Locate every malaria parasite.
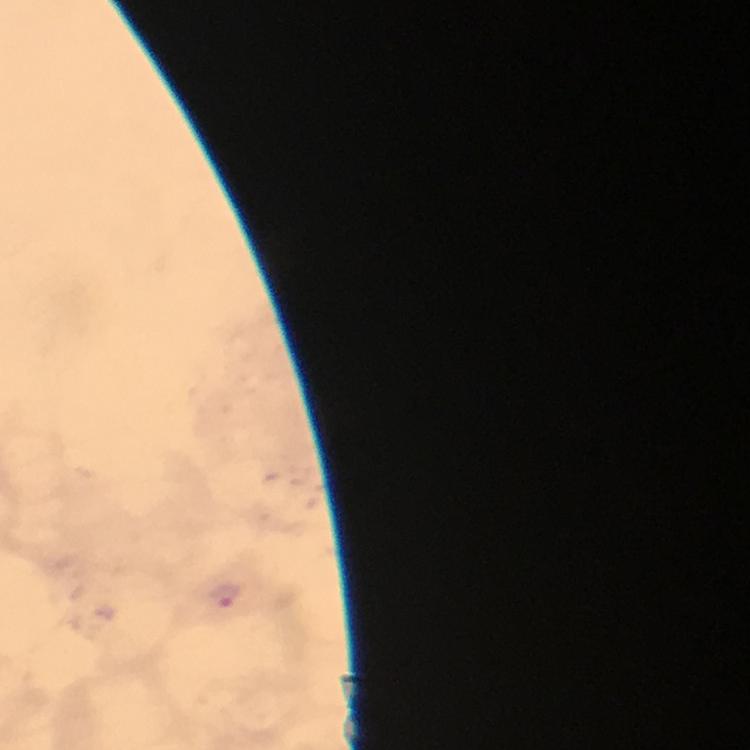
Approximate centers as {x, y} in pixels.
Malaria parasites: {225, 596}.

From a malaria diagnostic workup. Immersion oil was used. Thick blood smear. Photographed with a smartphone mounted on the microscope. Cropped region of a single field of view. At 100x magnification. Giemsa-stained preparation. Image is 750×750 pixels.